Assess this cell for malaria.
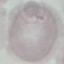

It is uninfected.

image type = automatically extracted cell patch, resized to 64 × 64 pixels
capture = smartphone camera at the microscope eyepiece
preparation = thin blood smear
stain = Giemsa